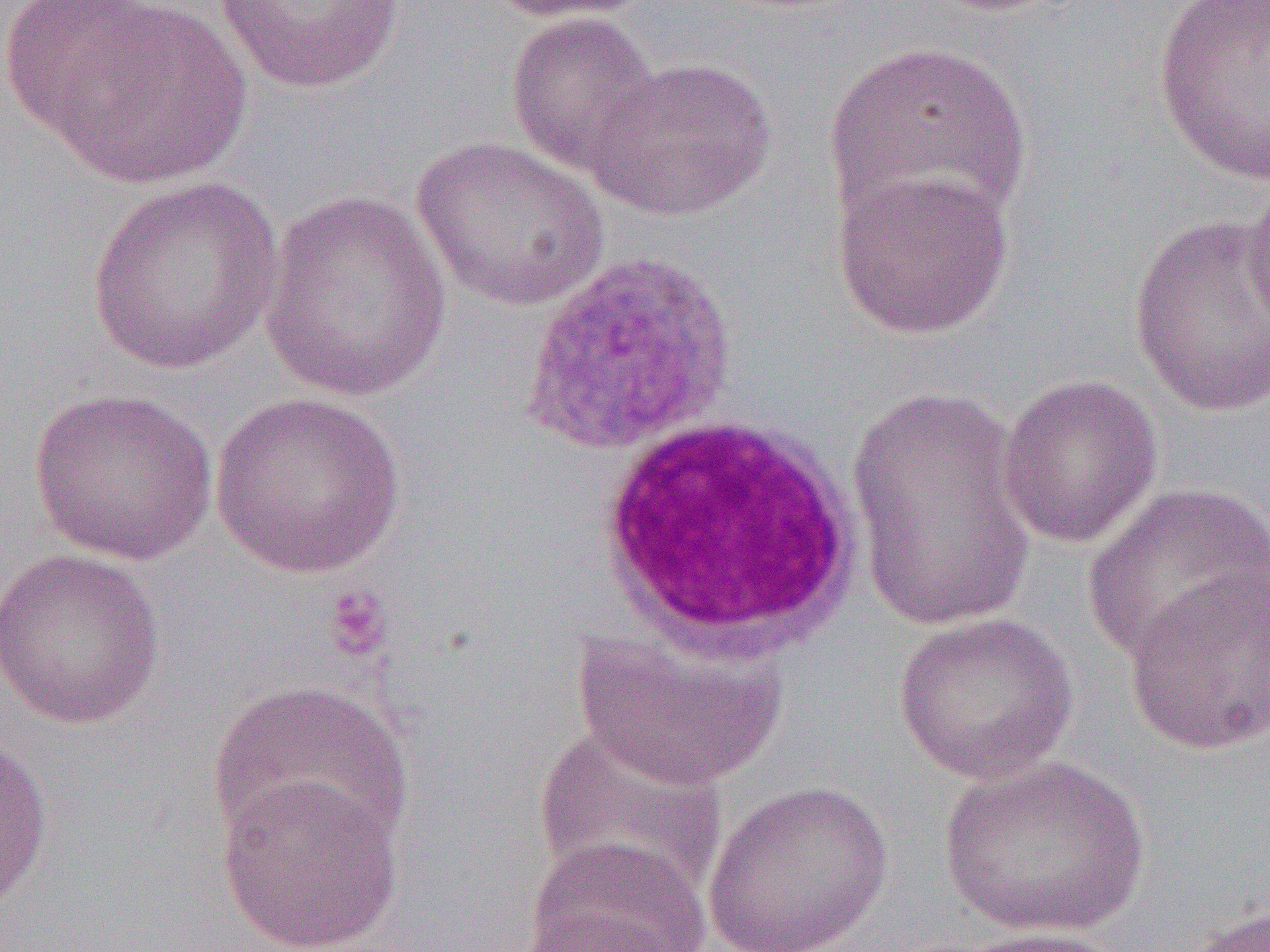

Approximate bounding boxes as (x1, y1, x2, y2) in pixels. Platelet locations: (320, 582, 395, 664). Uninfected red blood cell locations: (19, 0, 254, 189), (211, 0, 405, 95), (483, 0, 652, 24), (1153, 2, 1270, 185), (505, 10, 663, 178), (823, 39, 1035, 239), (586, 56, 778, 221), (409, 135, 611, 312), (830, 166, 1014, 341), (1243, 172, 1270, 340), (85, 177, 284, 376), (259, 190, 452, 403), (1127, 213, 1269, 417), (996, 373, 1164, 549), (846, 382, 1037, 637), (27, 387, 219, 566), (208, 390, 407, 578), (1081, 481, 1270, 667), (0, 547, 166, 730), (1123, 564, 1270, 757), (890, 612, 1078, 786), (572, 625, 787, 791), (206, 678, 412, 855), (532, 725, 726, 905), (0, 733, 53, 914), (937, 753, 1152, 938), (215, 771, 406, 952), (703, 780, 893, 952), (521, 835, 711, 952), (1183, 902, 1270, 952), (508, 913, 687, 952), (942, 926, 1133, 952). White blood cell locations: (590, 412, 867, 662). Plasmodium ovale-infected red blood cell locations: (519, 248, 740, 460). Slide-level diagnosis: Plasmodium ovale. One field of a larger specimen. 1000x magnification. Thin blood smear. Optical microscopy. Image is 1270×952 pixels.